Identify the blood parasite species.
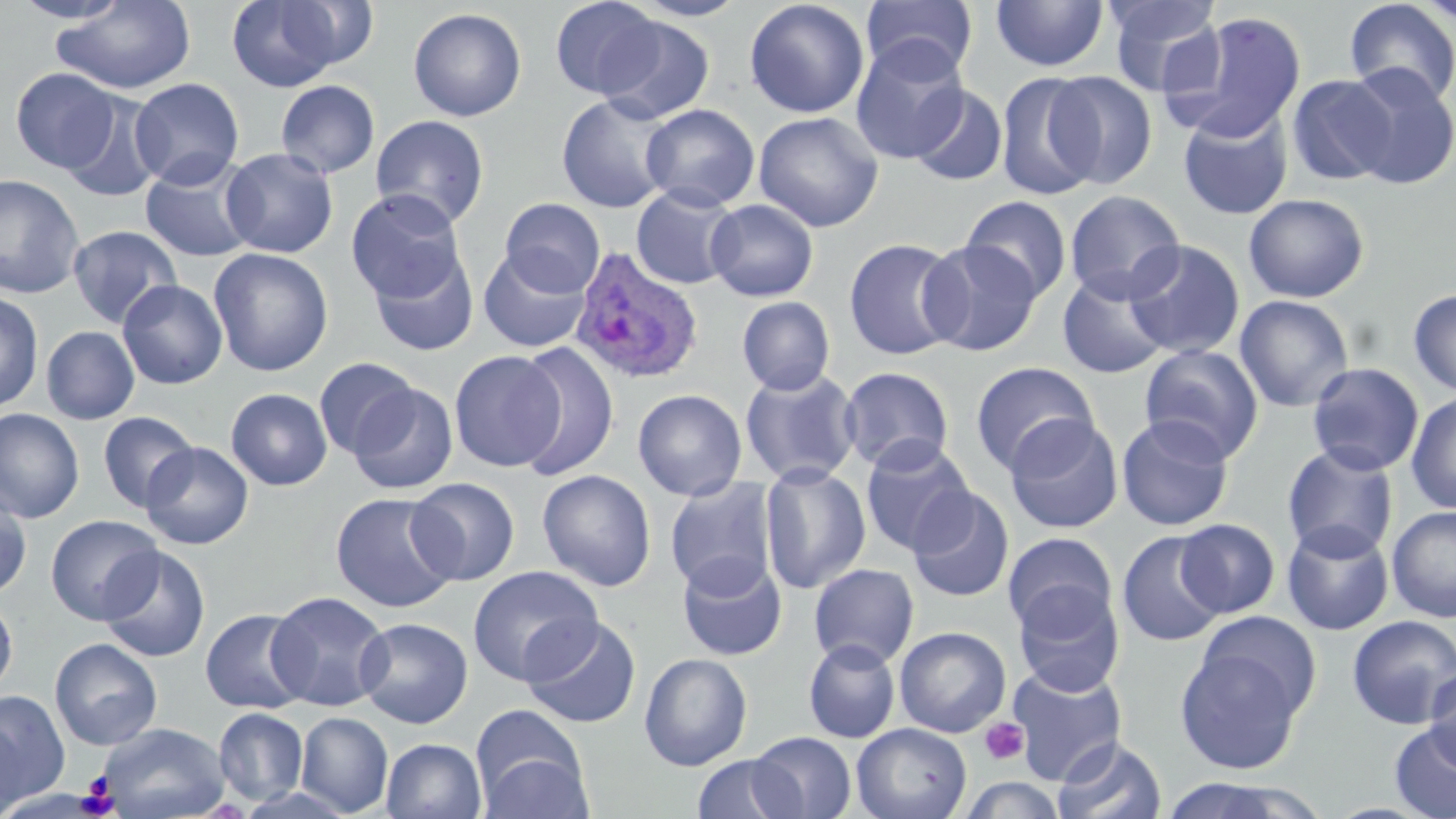
Plasmodium ovale.

uninfected red blood cell locations = approximate bounding boxes as (x1, y1, x2, y2) in pixels: (10, 0, 134, 24), (50, 0, 196, 95), (226, 0, 346, 92), (272, 0, 381, 71), (549, 0, 664, 99), (627, 0, 752, 22), (743, 0, 870, 118), (861, 0, 979, 81), (989, 0, 1109, 72), (1104, 0, 1226, 97), (1343, 0, 1456, 105), (407, 7, 527, 121), (1162, 12, 1307, 143), (597, 16, 716, 124), (849, 38, 970, 163), (1341, 63, 1456, 189), (10, 67, 120, 173), (995, 71, 1103, 200), (1046, 71, 1158, 189), (1287, 74, 1396, 186), (129, 78, 244, 188), (275, 79, 380, 178), (908, 85, 1008, 187), (61, 93, 166, 203), (557, 94, 677, 213), (640, 104, 760, 211), (1177, 108, 1293, 220), (753, 111, 884, 232), (371, 115, 489, 228), (221, 147, 338, 258), (140, 156, 259, 262), (0, 174, 84, 299), (631, 185, 742, 290), (346, 189, 467, 303), (1065, 190, 1185, 304), (1243, 193, 1370, 303), (961, 195, 1073, 302), (499, 198, 606, 296), (705, 199, 818, 302), (67, 225, 182, 328), (843, 237, 965, 360), (920, 239, 1043, 356), (1123, 241, 1245, 359), (208, 247, 334, 377), (478, 247, 593, 352), (368, 248, 479, 356), (1057, 270, 1172, 379), (117, 279, 228, 390), (1408, 288, 1456, 397), (0, 292, 44, 413), (1234, 294, 1355, 412), (737, 296, 835, 395), (41, 326, 140, 424), (511, 342, 620, 481), (1140, 344, 1263, 463), (448, 350, 565, 472), (313, 356, 420, 459), (970, 361, 1099, 476), (1306, 362, 1424, 475), (839, 366, 955, 473), (739, 367, 862, 487), (349, 383, 458, 495), (225, 388, 333, 490), (633, 388, 747, 501), (1406, 391, 1456, 515), (0, 408, 85, 523), (97, 411, 199, 512), (1004, 414, 1123, 534), (1117, 414, 1234, 531), (859, 437, 976, 556), (141, 442, 254, 550), (1282, 443, 1399, 561), (759, 463, 871, 595), (537, 469, 656, 591), (406, 477, 521, 586), (664, 477, 779, 597), (0, 486, 33, 598), (908, 486, 1015, 602), (328, 491, 461, 614), (1386, 505, 1456, 622), (45, 514, 163, 625), (1175, 518, 1280, 618), (1281, 521, 1394, 635), (1116, 530, 1227, 647), (1003, 532, 1118, 637), (98, 546, 210, 663), (676, 554, 788, 661), (808, 563, 919, 668), (467, 566, 603, 685), (1013, 583, 1125, 695), (266, 590, 393, 712), (0, 593, 17, 698), (199, 608, 313, 714), (1197, 611, 1322, 719), (1346, 615, 1456, 728), (354, 617, 473, 729), (521, 617, 642, 729), (894, 626, 1011, 737), (49, 638, 162, 750), (802, 639, 900, 743), (1175, 648, 1306, 774), (639, 652, 753, 770), (1007, 662, 1128, 785), (1424, 664, 1456, 774), (1, 690, 69, 804), (470, 703, 590, 815), (213, 708, 309, 805), (295, 711, 393, 817), (0, 717, 26, 819), (1389, 721, 1456, 819), (98, 722, 230, 819), (851, 723, 972, 819), (748, 732, 857, 819), (1052, 736, 1168, 819), (381, 738, 487, 819), (692, 753, 802, 818), (959, 775, 1069, 819), (1157, 777, 1331, 819)
platelet locations = approximate bounding boxes as (x1, y1, x2, y2) in pixels: (980, 718, 1029, 765), (80, 771, 117, 810)
modality = light microscopy
field of view = one of a larger specimen
preparation = thin blood film
image size = 1456×819 pixels
stain = May-Grünwald-Giemsa
Plasmodium ovale-infected red blood cell locations = approximate bounding boxes as (x1, y1, x2, y2) in pixels: (569, 246, 704, 385)
magnification = 1000x